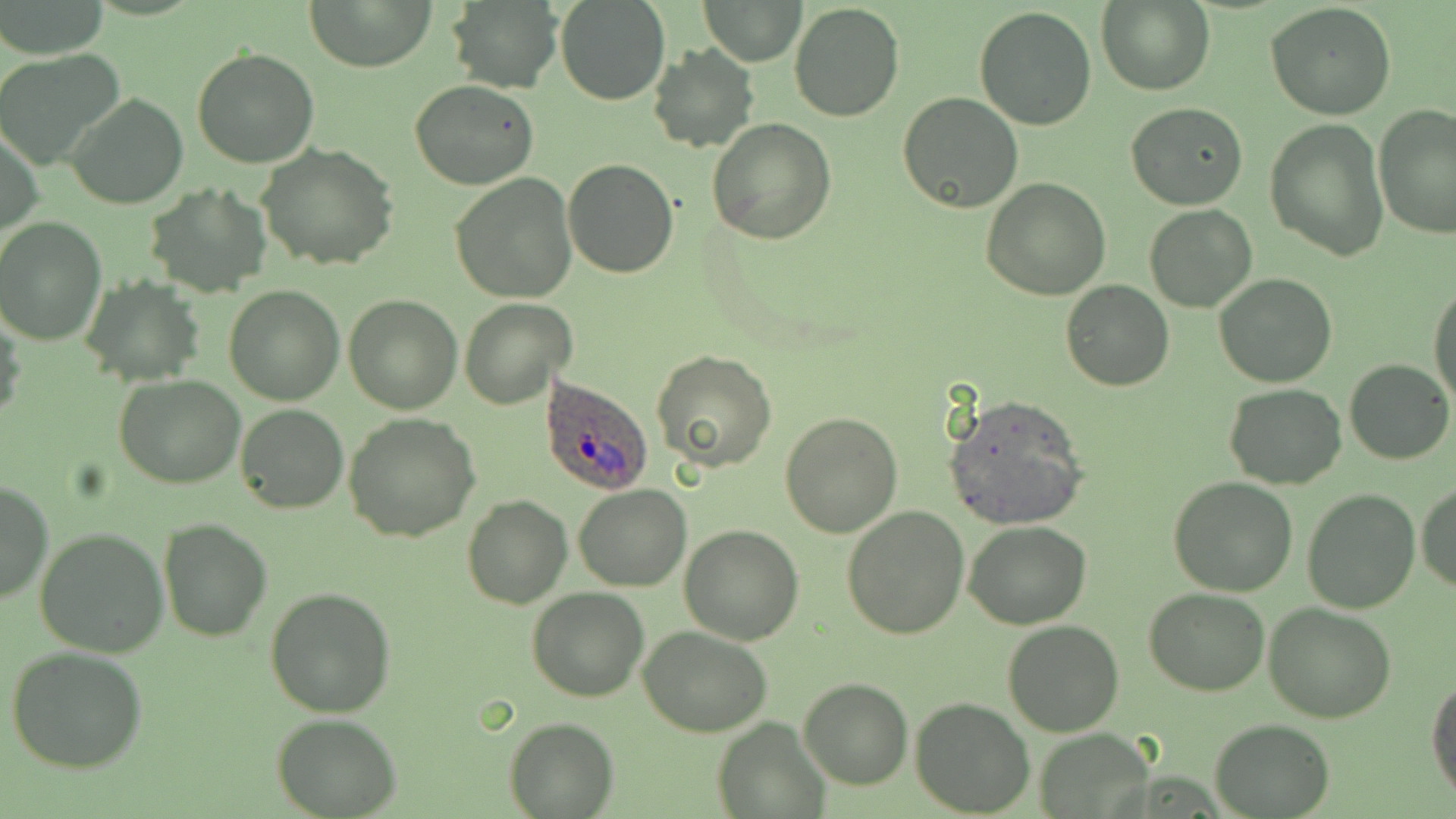

Summary:
  - Coordinate format: approximate bounding boxes as named x1/y1/x2/y2 corners in pixels
  - Uninfected red blood cell locations: (x1=308, y1=0, x2=435, y2=72), (x1=444, y1=0, x2=564, y2=93), (x1=556, y1=0, x2=670, y2=105), (x1=2, y1=1, x2=108, y2=59), (x1=699, y1=1, x2=806, y2=65), (x1=789, y1=1, x2=904, y2=120), (x1=1096, y1=1, x2=1216, y2=96), (x1=1265, y1=2, x2=1396, y2=120), (x1=974, y1=6, x2=1096, y2=131), (x1=647, y1=44, x2=759, y2=152), (x1=192, y1=47, x2=320, y2=168), (x1=0, y1=49, x2=125, y2=169), (x1=408, y1=80, x2=540, y2=190), (x1=897, y1=90, x2=1023, y2=214), (x1=64, y1=92, x2=188, y2=210), (x1=1125, y1=102, x2=1249, y2=210), (x1=1373, y1=104, x2=1455, y2=237), (x1=707, y1=119, x2=836, y2=244), (x1=1265, y1=119, x2=1388, y2=262), (x1=1, y1=123, x2=43, y2=242), (x1=258, y1=143, x2=399, y2=270), (x1=564, y1=158, x2=679, y2=278), (x1=450, y1=174, x2=577, y2=302), (x1=981, y1=179, x2=1112, y2=300), (x1=145, y1=183, x2=270, y2=295), (x1=1144, y1=204, x2=1257, y2=313), (x1=0, y1=218, x2=106, y2=345), (x1=1214, y1=274, x2=1339, y2=389), (x1=81, y1=278, x2=205, y2=386), (x1=1060, y1=279, x2=1174, y2=392), (x1=1428, y1=280, x2=1455, y2=406), (x1=225, y1=285, x2=345, y2=405), (x1=343, y1=293, x2=463, y2=414), (x1=460, y1=297, x2=577, y2=410), (x1=1, y1=307, x2=23, y2=427), (x1=652, y1=349, x2=777, y2=472), (x1=1345, y1=359, x2=1453, y2=465), (x1=114, y1=374, x2=245, y2=488), (x1=1225, y1=382, x2=1345, y2=488), (x1=943, y1=395, x2=1089, y2=530), (x1=236, y1=403, x2=348, y2=513), (x1=779, y1=411, x2=904, y2=536), (x1=344, y1=414, x2=480, y2=541), (x1=1167, y1=476, x2=1298, y2=596), (x1=1, y1=480, x2=51, y2=606), (x1=1414, y1=480, x2=1456, y2=592), (x1=572, y1=485, x2=691, y2=590), (x1=1302, y1=490, x2=1418, y2=613), (x1=462, y1=494, x2=572, y2=609), (x1=842, y1=505, x2=969, y2=640), (x1=158, y1=517, x2=271, y2=641), (x1=964, y1=522, x2=1092, y2=629), (x1=681, y1=525, x2=803, y2=644), (x1=33, y1=526, x2=168, y2=659), (x1=527, y1=586, x2=649, y2=701), (x1=1145, y1=587, x2=1271, y2=696), (x1=265, y1=588, x2=396, y2=717), (x1=1262, y1=601, x2=1396, y2=723), (x1=1003, y1=618, x2=1124, y2=736), (x1=640, y1=626, x2=771, y2=736), (x1=5, y1=645, x2=151, y2=773), (x1=1427, y1=676, x2=1456, y2=804), (x1=798, y1=678, x2=913, y2=789), (x1=910, y1=697, x2=1035, y2=817), (x1=273, y1=713, x2=401, y2=817), (x1=504, y1=716, x2=617, y2=818), (x1=713, y1=716, x2=828, y2=816), (x1=1209, y1=718, x2=1334, y2=817), (x1=1033, y1=727, x2=1157, y2=818)
  - Plasmodium ovale-infected red blood cell locations: (x1=540, y1=374, x2=654, y2=494)
  - Slide-level diagnosis: Plasmodium ovale
  - Stain: May-Grünwald-Giemsa
  - Preparation: thin blood smear
  - Modality: optical microscopy
  - Field of view: one of a larger specimen
  - Image size: 1456×819 pixels
  - Magnification: 1000x